Outline each blood parasite and name the species.
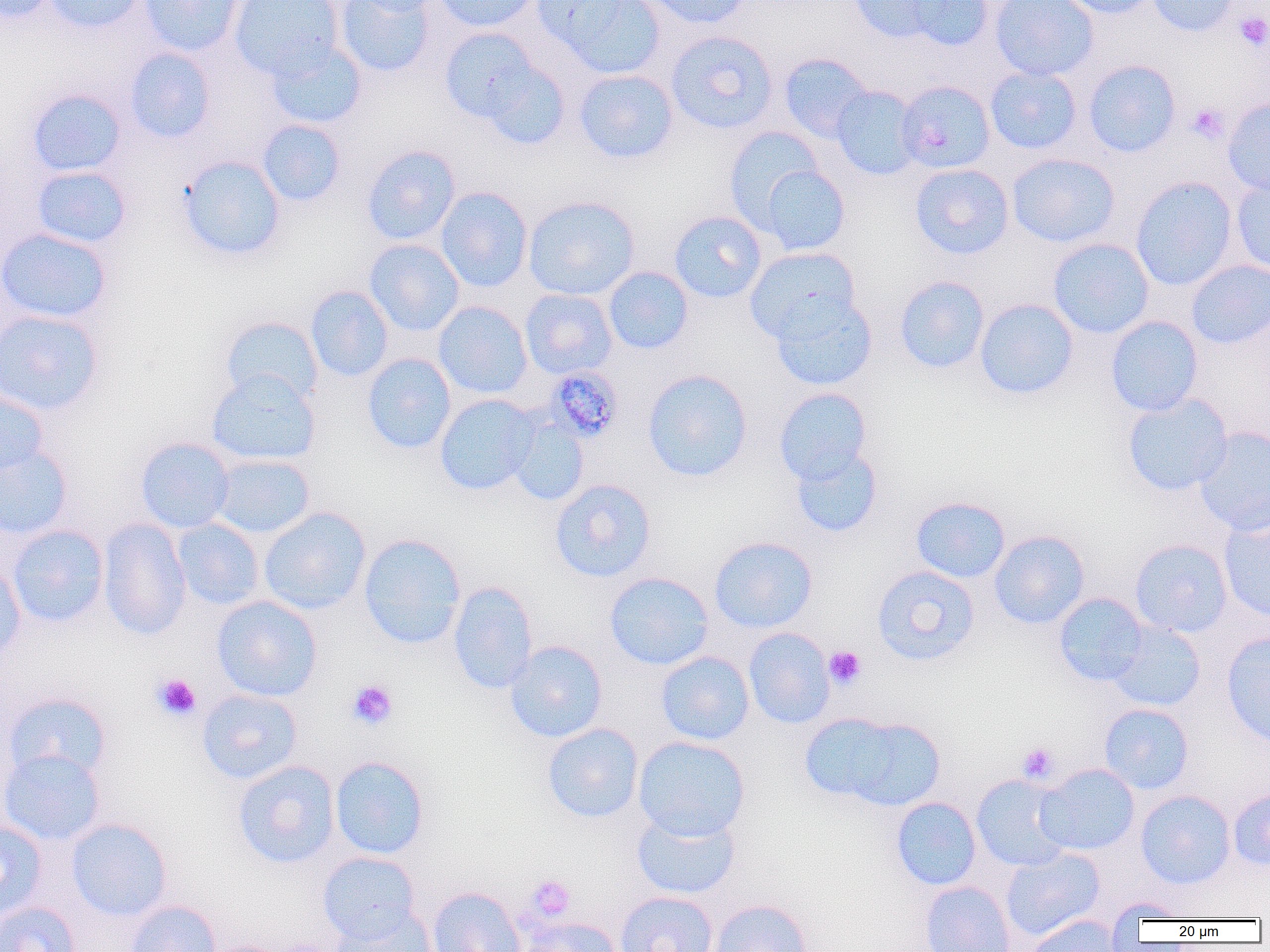
Approximate bounding boxes as named x1/y1/x2/y2 corners in pixels.
Plasmodium malariae-infected red blood cells: (x1=544, y1=366, x2=625, y2=443).
No Plasmodium falciparum, Plasmodium ovale, Plasmodium vivax, Babesia divergens, or Trypanosoma brucei observed.

Uninfected red blood cell locations: (x1=1, y1=0, x2=58, y2=24), (x1=44, y1=0, x2=144, y2=33), (x1=138, y1=0, x2=242, y2=57), (x1=231, y1=0, x2=344, y2=79), (x1=335, y1=0, x2=436, y2=77), (x1=355, y1=0, x2=442, y2=16), (x1=432, y1=0, x2=541, y2=32), (x1=537, y1=0, x2=666, y2=79), (x1=641, y1=0, x2=751, y2=29), (x1=848, y1=0, x2=955, y2=45), (x1=899, y1=0, x2=995, y2=51), (x1=990, y1=0, x2=1099, y2=81), (x1=1057, y1=0, x2=1161, y2=18), (x1=1148, y1=0, x2=1239, y2=37), (x1=439, y1=25, x2=561, y2=136), (x1=665, y1=30, x2=778, y2=135), (x1=265, y1=39, x2=367, y2=129), (x1=124, y1=47, x2=216, y2=143), (x1=779, y1=53, x2=874, y2=143), (x1=1083, y1=59, x2=1181, y2=158), (x1=985, y1=65, x2=1082, y2=154), (x1=574, y1=69, x2=678, y2=164), (x1=896, y1=80, x2=996, y2=173), (x1=831, y1=86, x2=923, y2=180), (x1=27, y1=88, x2=126, y2=177), (x1=1223, y1=98, x2=1270, y2=197), (x1=257, y1=119, x2=345, y2=206), (x1=723, y1=126, x2=825, y2=232), (x1=361, y1=145, x2=460, y2=245), (x1=1007, y1=153, x2=1119, y2=247), (x1=179, y1=155, x2=286, y2=261), (x1=758, y1=164, x2=850, y2=255), (x1=910, y1=164, x2=1014, y2=259), (x1=32, y1=166, x2=132, y2=249), (x1=1130, y1=176, x2=1237, y2=291), (x1=1231, y1=176, x2=1270, y2=274), (x1=435, y1=187, x2=533, y2=291), (x1=523, y1=195, x2=640, y2=300), (x1=669, y1=211, x2=767, y2=303), (x1=1, y1=228, x2=112, y2=324), (x1=1048, y1=238, x2=1154, y2=338), (x1=364, y1=239, x2=464, y2=336), (x1=745, y1=247, x2=860, y2=343), (x1=1186, y1=260, x2=1270, y2=348), (x1=604, y1=266, x2=693, y2=354), (x1=894, y1=275, x2=990, y2=374), (x1=305, y1=285, x2=393, y2=382), (x1=520, y1=288, x2=618, y2=379), (x1=771, y1=296, x2=877, y2=391), (x1=975, y1=298, x2=1079, y2=399), (x1=433, y1=301, x2=532, y2=399), (x1=0, y1=309, x2=103, y2=416), (x1=1105, y1=315, x2=1204, y2=416), (x1=220, y1=316, x2=323, y2=406), (x1=362, y1=353, x2=456, y2=454), (x1=642, y1=369, x2=753, y2=483), (x1=207, y1=371, x2=321, y2=465), (x1=774, y1=388, x2=872, y2=484), (x1=0, y1=390, x2=48, y2=479), (x1=1122, y1=393, x2=1232, y2=496), (x1=434, y1=394, x2=540, y2=495), (x1=508, y1=415, x2=590, y2=506), (x1=1194, y1=426, x2=1270, y2=536), (x1=135, y1=437, x2=235, y2=533), (x1=790, y1=445, x2=884, y2=538), (x1=0, y1=446, x2=72, y2=540), (x1=210, y1=454, x2=316, y2=538), (x1=549, y1=478, x2=656, y2=583), (x1=910, y1=496, x2=1010, y2=583), (x1=258, y1=506, x2=371, y2=614), (x1=1219, y1=513, x2=1270, y2=622), (x1=98, y1=518, x2=191, y2=641), (x1=172, y1=518, x2=265, y2=610), (x1=6, y1=524, x2=109, y2=627), (x1=989, y1=530, x2=1089, y2=629), (x1=359, y1=533, x2=466, y2=649), (x1=708, y1=536, x2=818, y2=633), (x1=1130, y1=538, x2=1233, y2=637), (x1=0, y1=557, x2=26, y2=663), (x1=871, y1=565, x2=980, y2=666), (x1=604, y1=571, x2=714, y2=670), (x1=447, y1=581, x2=539, y2=693), (x1=1053, y1=592, x2=1150, y2=686), (x1=211, y1=595, x2=322, y2=701), (x1=1105, y1=620, x2=1206, y2=712), (x1=743, y1=628, x2=835, y2=729), (x1=1221, y1=632, x2=1270, y2=748), (x1=505, y1=640, x2=608, y2=742), (x1=656, y1=651, x2=754, y2=745), (x1=196, y1=688, x2=303, y2=784), (x1=3, y1=692, x2=112, y2=784), (x1=1099, y1=703, x2=1193, y2=794), (x1=799, y1=710, x2=942, y2=811), (x1=542, y1=723, x2=644, y2=824), (x1=633, y1=736, x2=750, y2=840), (x1=0, y1=749, x2=106, y2=846), (x1=329, y1=755, x2=429, y2=859), (x1=232, y1=760, x2=340, y2=868), (x1=1036, y1=763, x2=1139, y2=855), (x1=971, y1=774, x2=1073, y2=871), (x1=1228, y1=788, x2=1270, y2=870), (x1=1135, y1=790, x2=1236, y2=889), (x1=891, y1=796, x2=982, y2=890), (x1=631, y1=808, x2=741, y2=900), (x1=66, y1=818, x2=172, y2=921), (x1=0, y1=820, x2=47, y2=920), (x1=1001, y1=847, x2=1105, y2=940), (x1=317, y1=851, x2=421, y2=942), (x1=919, y1=880, x2=1015, y2=952), (x1=427, y1=886, x2=526, y2=952), (x1=614, y1=891, x2=718, y2=952), (x1=1106, y1=897, x2=1189, y2=925), (x1=709, y1=898, x2=814, y2=952), (x1=125, y1=900, x2=221, y2=952), (x1=0, y1=901, x2=80, y2=952), (x1=329, y1=904, x2=437, y2=952), (x1=1021, y1=913, x2=1125, y2=952), (x1=517, y1=916, x2=623, y2=952). Platelet locations: (x1=1234, y1=11, x2=1270, y2=51), (x1=1186, y1=103, x2=1230, y2=144), (x1=824, y1=646, x2=866, y2=689), (x1=151, y1=673, x2=201, y2=721), (x1=346, y1=679, x2=398, y2=729), (x1=1017, y1=742, x2=1059, y2=784), (x1=526, y1=875, x2=575, y2=921). Slide-level diagnosis: Plasmodium malariae. Thin blood film. Light microscopy. Image is 1270×952 pixels. One field of a larger specimen. 1000x magnification.